Name the cell type shown.
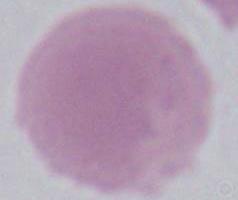
An erythrocyte.

Summary:
  - Modality: micrograph
  - Magnification: 1000x